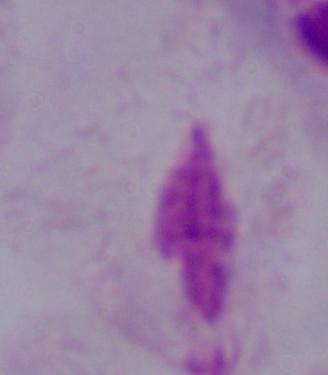

Summary:
  - Magnification: 1000x
  - Identification: trichomonad
  - Modality: micrograph